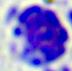

{
  "identification": "leukocyte",
  "modality": "photomicrograph",
  "magnification": "400x"
}